Report the malaria status of this cell.
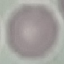

It is uninfected.

stain = Giemsa
capture = smartphone camera at the microscope eyepiece
image type = automatically extracted cell patch, resized to 64 × 64 pixels
preparation = thin blood smear